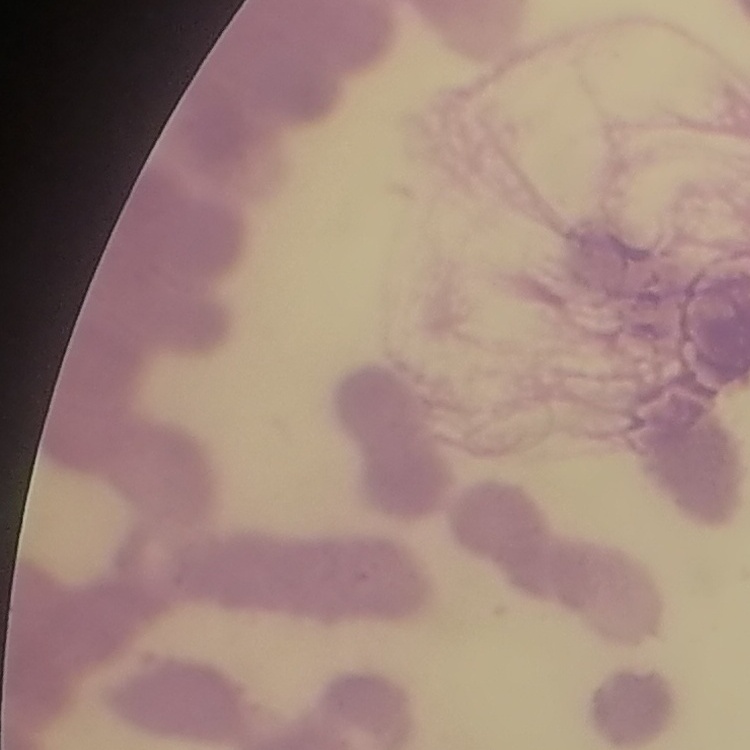

The red blood cells exhibit rouleaux formation. Square crop of a larger photomicrograph. Thin peripheral smear. Field's or Giemsa stain.